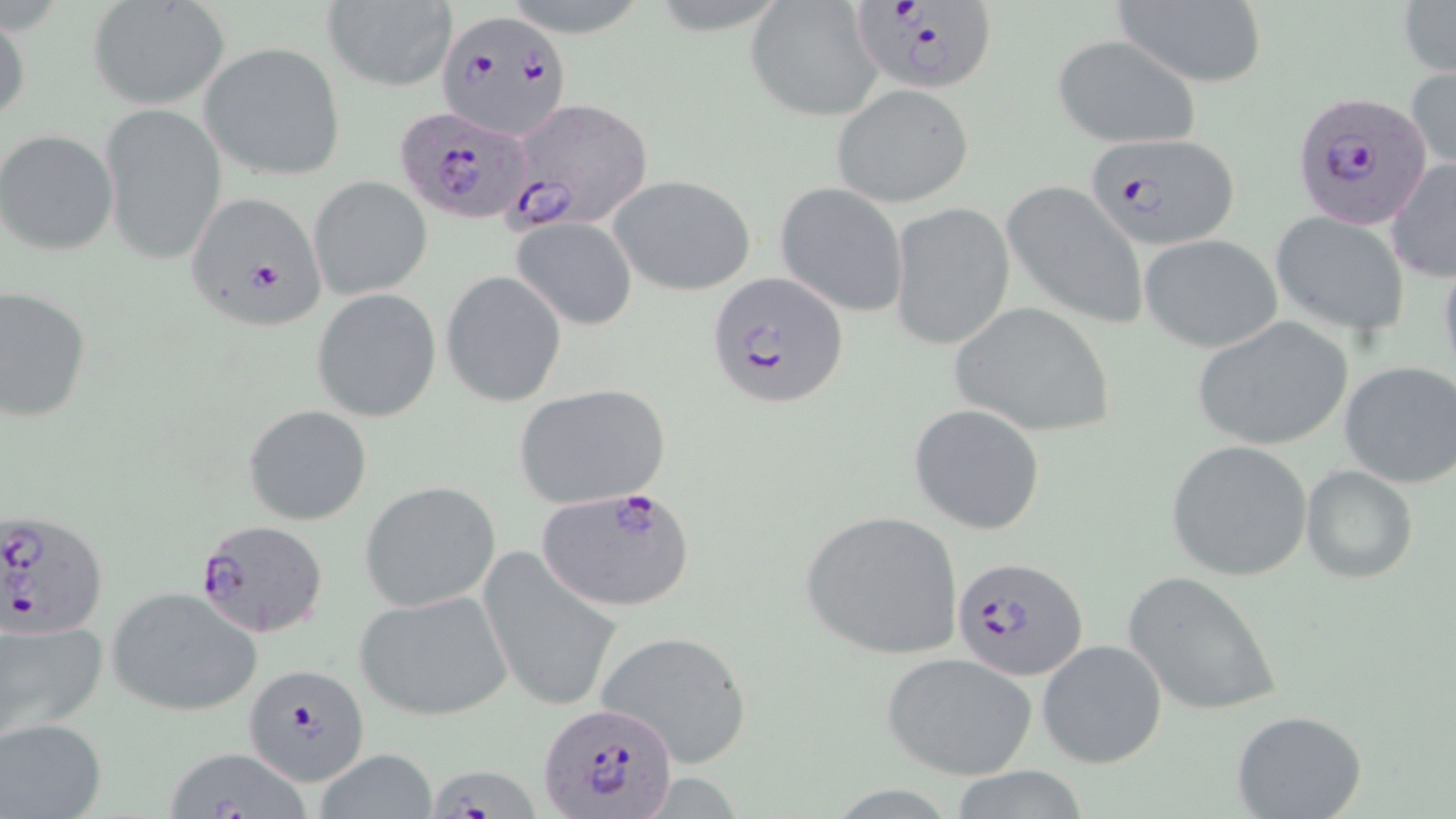
slide-level diagnosis = Plasmodium falciparum
modality = light microscopy
image size = 1456×819 pixels
field of view = one of a larger specimen
uninfected red blood cell locations = approximate bounding boxes as (x1,y1)-(x2,y2) corner pairs in pixels: (320,1)-(456,92), (1110,1)-(1268,87), (1397,1)-(1456,81), (87,2)-(231,111), (745,3)-(882,121), (0,7)-(30,131), (1050,34)-(1203,150), (199,41)-(346,181), (1406,65)-(1455,177), (830,83)-(974,207), (99,101)-(225,269), (1,131)-(119,255), (1386,157)-(1456,281), (609,173)-(758,295), (308,176)-(432,300), (1002,180)-(1149,332), (776,183)-(910,316), (889,202)-(1015,351), (1270,212)-(1411,338), (512,216)-(638,331), (1139,234)-(1282,352), (440,270)-(567,407), (1,286)-(92,424), (311,289)-(441,422), (949,301)-(1115,437), (1191,317)-(1356,451), (1338,361)-(1456,488), (514,383)-(671,509), (909,403)-(1047,536), (245,405)-(371,526), (1166,439)-(1315,581), (1300,464)-(1418,583), (359,480)-(501,611), (800,509)-(964,661), (478,549)-(627,714), (1122,568)-(1284,718), (106,585)-(262,715), (354,588)-(516,722), (0,613)-(108,744), (596,630)-(754,769), (1036,638)-(1168,770), (881,653)-(1037,780), (1230,711)-(1369,819), (1,717)-(107,818), (163,746)-(313,818), (318,748)-(436,819)
Plasmodium falciparum-infected red blood cell locations = approximate bounding boxes as (x1,y1)-(x2,y2) corner pairs in pixels: (851,3)-(995,92), (437,7)-(573,140), (1290,90)-(1435,230), (504,97)-(653,229), (397,106)-(533,224), (1081,131)-(1236,250), (186,191)-(330,329), (707,272)-(850,407), (534,487)-(694,612), (1,508)-(107,644), (194,518)-(331,638), (952,555)-(1087,679), (245,658)-(373,783), (538,701)-(678,815), (428,767)-(547,819)
stain = May-Grünwald-Giemsa
magnification = 1000x
preparation = thin blood smear